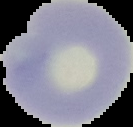 From a thin blood smear. Image is 133×127 pixels. Segmented cell region on a black background. Result: no Plasmodium parasites seen.